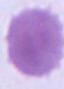

Summary:
  - Identification: erythrocyte
  - Modality: photomicrograph
  - Magnification: 1000x